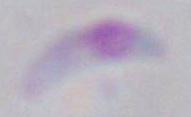

identification = Toxoplasma gondii
modality = photomicrograph
magnification = 1000x